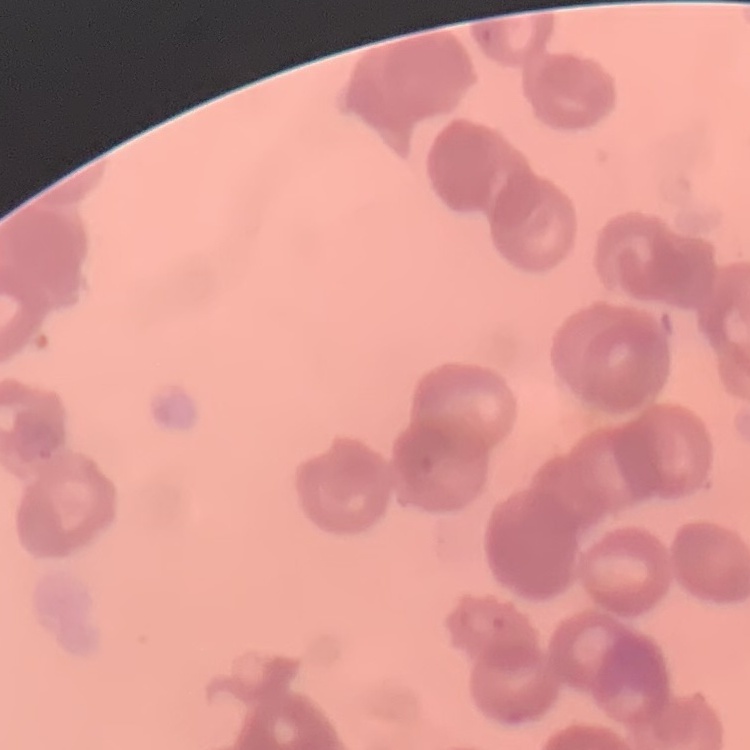
The red blood cells show rouleaux formation. Field's or Giemsa stain. Thin blood smear. One tile cut from a larger photomicrograph.